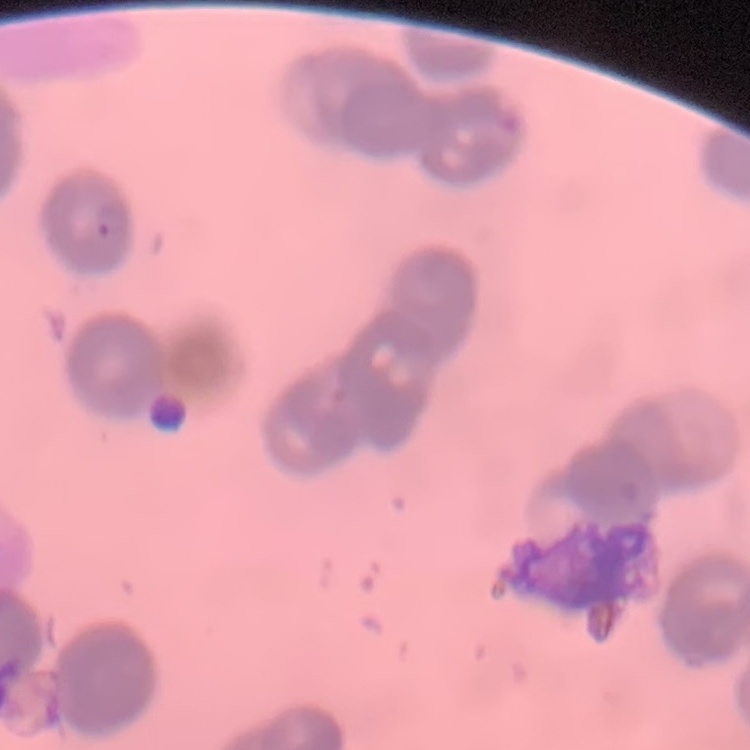

red blood cell morphology = rouleaux formation
stain = Field's or Giemsa
image type = square crop of a larger photomicrograph
preparation = thin blood film